Classify this cell by malaria status.
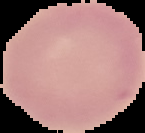

Uninfected.

Image is 145×133 pixels. Cell region segmented out of the field of view; the surrounding area is masked to black. From a thin blood film.